Assess this cell for malaria.
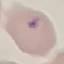

Parasitized.

image type = cell patch, automatically extracted from a larger field of view and resized to 64 × 64 pixels
preparation = thin smear
capture = smartphone camera at the microscope eyepiece
stain = Giemsa